Report the malaria status of this cell.
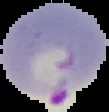
Parasitized.

Summary:
  - Image type: segmented cell region with the area outside set to black
  - Image size: 109×112 pixels
  - Preparation: thin blood smear